Outline each blood parasite and name the species.
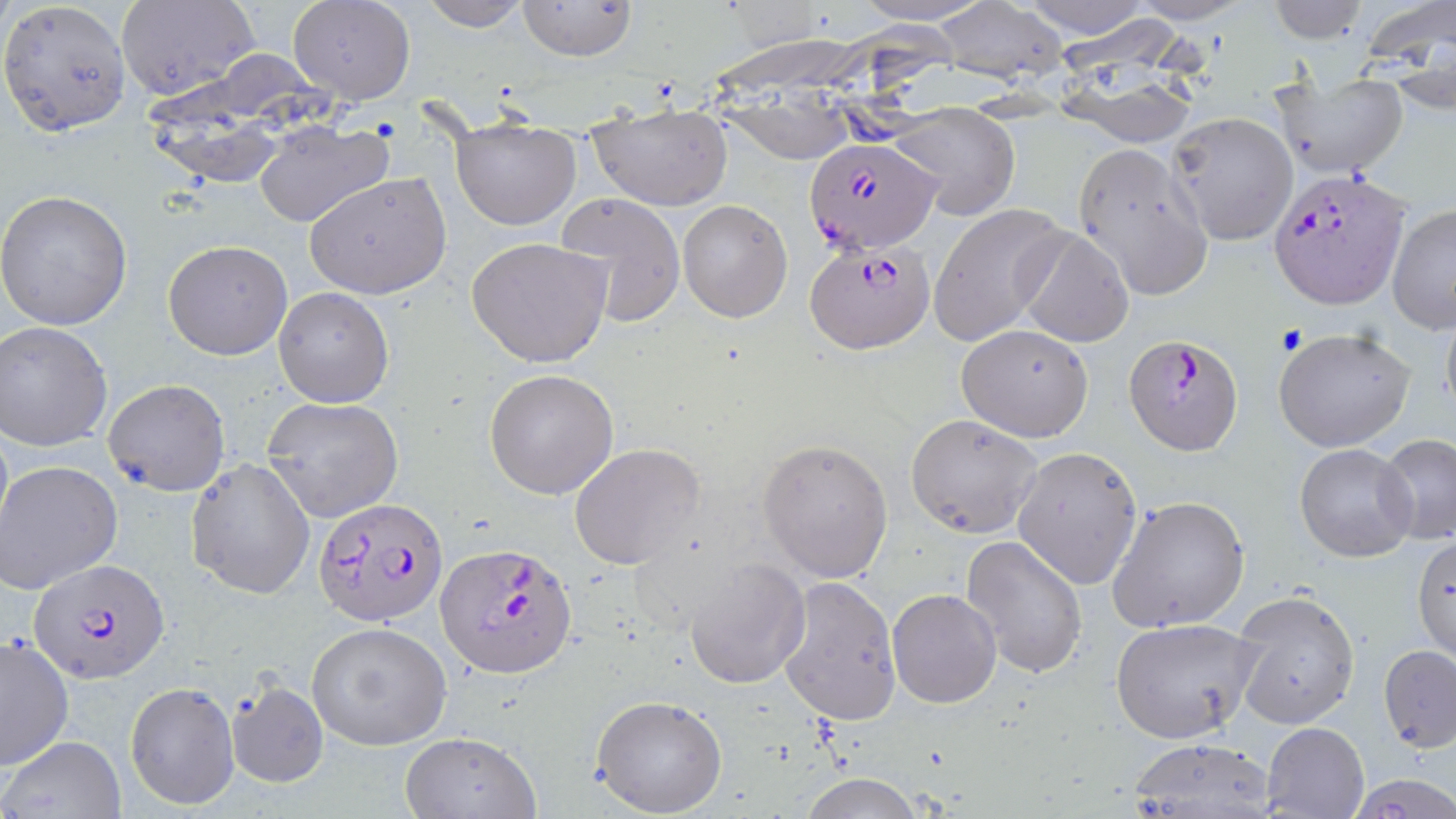
Approximate bounding boxes as [x1, y1, x2, y2] in pixels.
Plasmodium falciparum-infected red blood cells: [803, 136, 940, 253], [1269, 168, 1408, 308], [806, 241, 936, 352], [1124, 333, 1242, 455], [314, 496, 449, 626], [435, 541, 579, 680], [29, 558, 168, 683].
No Plasmodium ovale, Plasmodium malariae, Plasmodium vivax, Babesia divergens, or Trypanosoma brucei observed.

Uninfected red blood cell locations: [0, 0, 132, 137], [288, 0, 416, 105], [1263, 0, 1371, 44], [1354, 0, 1456, 108], [116, 1, 257, 101], [418, 1, 531, 30], [515, 1, 636, 61], [934, 4, 1063, 82], [716, 30, 870, 170], [1054, 62, 1202, 147], [1267, 71, 1409, 178], [588, 99, 734, 212], [891, 103, 1019, 219], [154, 105, 298, 190], [1165, 111, 1298, 246], [450, 116, 582, 230], [254, 121, 393, 230], [1071, 142, 1213, 302], [303, 172, 451, 300], [0, 188, 133, 330], [556, 192, 686, 327], [677, 200, 794, 321], [932, 203, 1069, 347], [1386, 203, 1456, 334], [1016, 227, 1134, 349], [466, 237, 612, 370], [163, 240, 293, 359], [274, 287, 394, 408], [1440, 303, 1456, 425], [1, 319, 116, 451], [957, 323, 1094, 441], [1273, 327, 1415, 452], [483, 368, 620, 500], [102, 378, 231, 495], [263, 396, 404, 522], [905, 414, 1043, 538], [1375, 433, 1456, 545], [756, 437, 895, 582], [570, 444, 707, 571], [1295, 444, 1418, 562], [1012, 446, 1144, 590], [184, 457, 315, 599], [0, 459, 124, 595], [1107, 494, 1250, 633], [959, 533, 1088, 679], [1413, 533, 1455, 665], [684, 557, 810, 688], [776, 575, 902, 725], [886, 588, 1003, 709], [1232, 590, 1360, 729], [1110, 617, 1261, 743], [306, 621, 452, 750], [1, 632, 73, 771], [1379, 645, 1455, 753], [124, 679, 239, 810], [228, 680, 329, 788], [592, 694, 727, 817], [1261, 721, 1369, 818], [398, 731, 540, 818], [2, 735, 126, 817], [1128, 738, 1279, 816], [800, 773, 923, 819], [1351, 777, 1456, 816]. Slide-level diagnosis: Plasmodium falciparum. Optical microscopy. Single field of view. 1000x magnification. May-Grünwald-Giemsa stain. Thin blood film. Image is 1456×819 pixels.